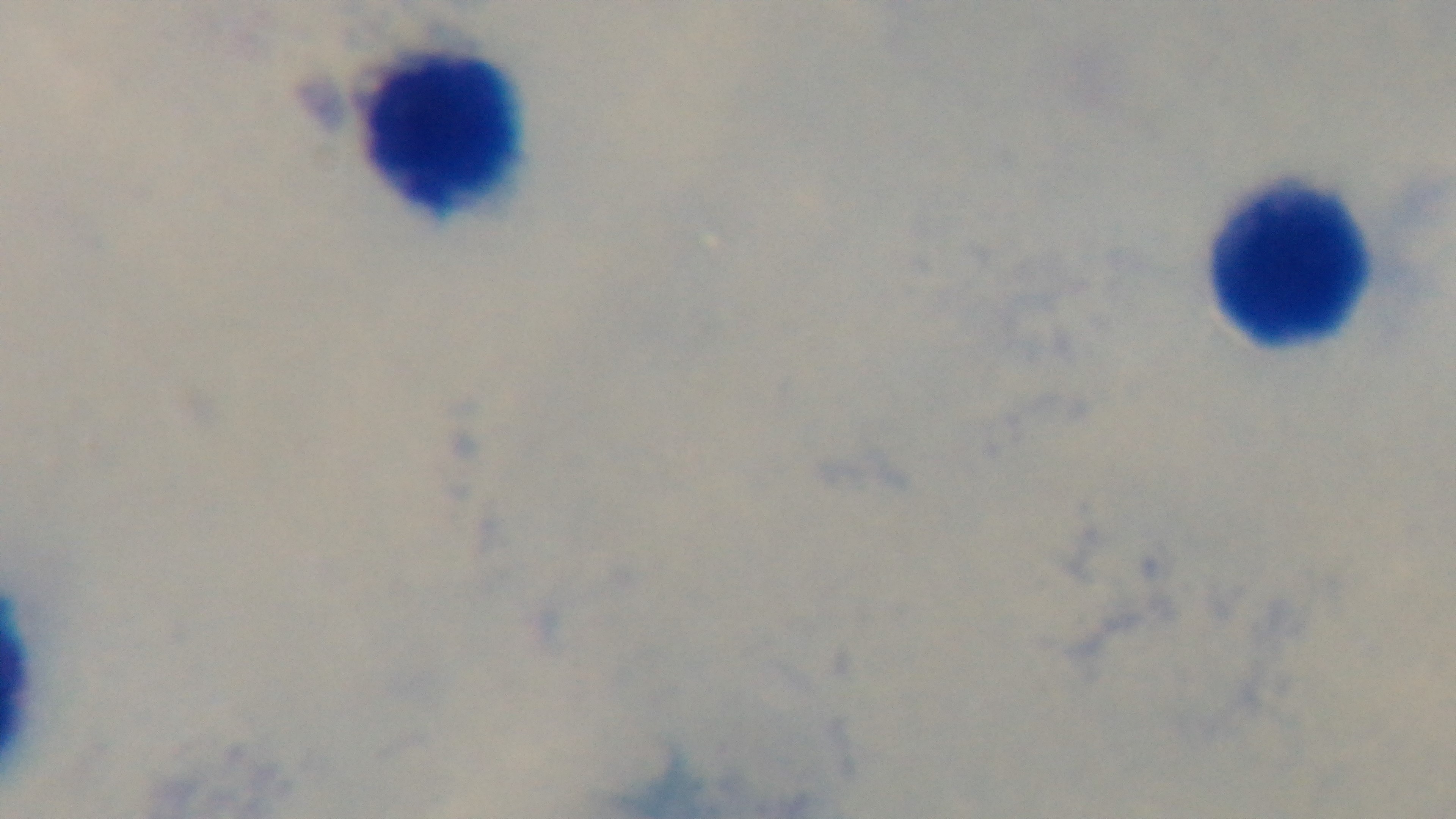

Captured with a mounted 4K digital camera. Photomicrograph. Oil-immersion objective, 100x. One field from the slide. Malaria status: uninfected. Preparation: thick. Giemsa stain.